Report the malaria status of this cell.
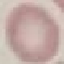

It is uninfected.

Thin blood smear. Giemsa-stained preparation. Cell patch, automatically extracted from a larger field of view and resized to 64 × 64 pixels. Photographed with a smartphone camera at the microscope eyepiece.